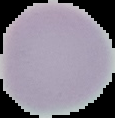
image type = segmented cell region on a black background
image size = 115×118 pixels
malaria status = uninfected
preparation = thin blood film